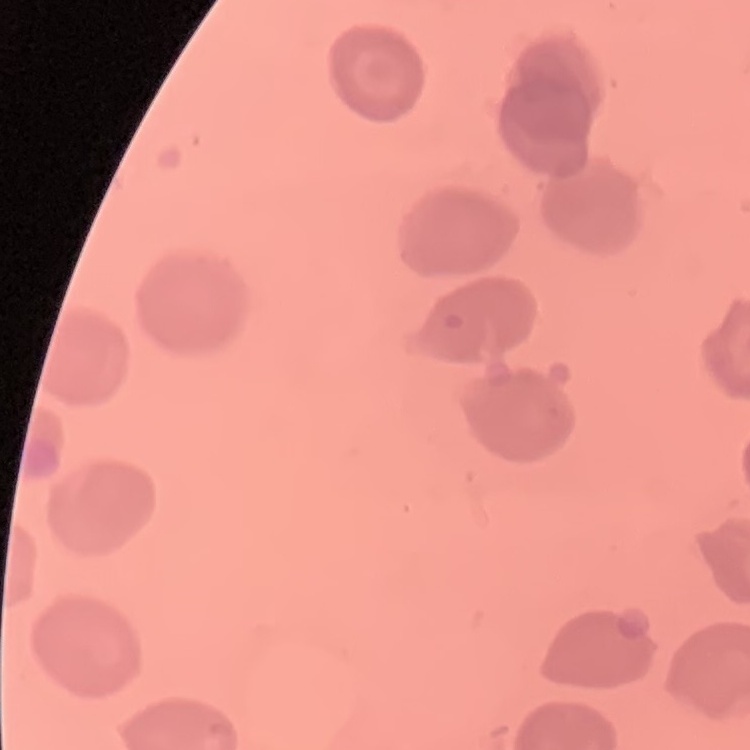

Summary:
  - Red blood cell morphology: no rouleaux formation
  - Stain: Field's or Giemsa
  - Preparation: thin peripheral smear
  - Image type: square crop of a larger photomicrograph